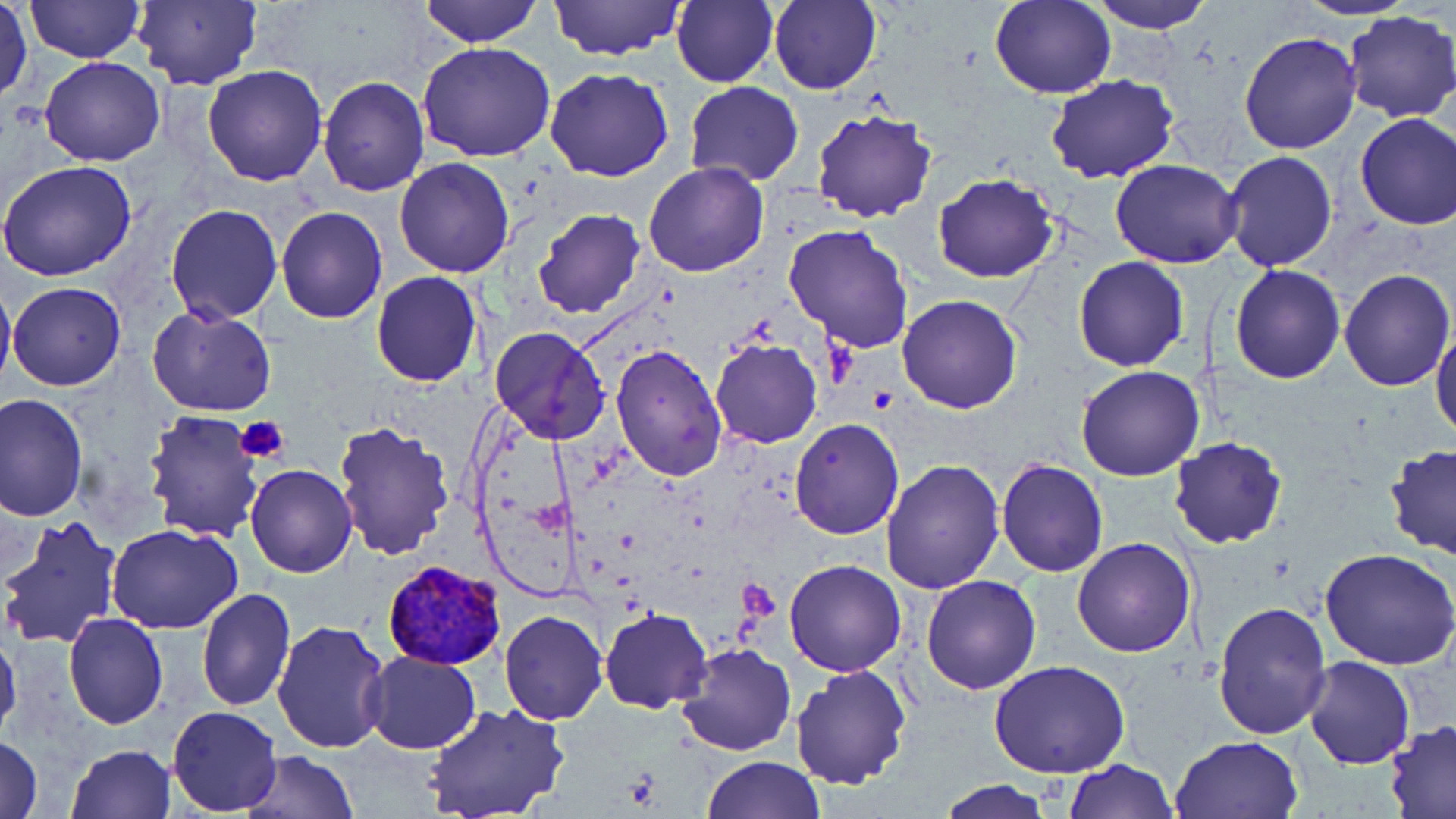
Summary:
  - Coordinate format: approximate bounding boxes as named x1/y1/x2/y2 corners in pixels
  - Plasmodium vivax-infected red blood cell locations: (x1=382, y1=561, x2=506, y2=671)
  - Platelet locations: (x1=235, y1=414, x2=290, y2=466), (x1=737, y1=576, x2=781, y2=620)
  - Uninfected red blood cell locations: (x1=23, y1=0, x2=145, y2=65), (x1=419, y1=0, x2=542, y2=47), (x1=548, y1=0, x2=685, y2=61), (x1=671, y1=0, x2=778, y2=88), (x1=989, y1=0, x2=1116, y2=99), (x1=1090, y1=0, x2=1217, y2=33), (x1=1295, y1=0, x2=1414, y2=22), (x1=131, y1=1, x2=263, y2=89), (x1=769, y1=1, x2=880, y2=94), (x1=1, y1=5, x2=33, y2=104), (x1=1343, y1=10, x2=1456, y2=124), (x1=1237, y1=32, x2=1363, y2=156), (x1=417, y1=42, x2=557, y2=162), (x1=38, y1=57, x2=166, y2=167), (x1=202, y1=64, x2=328, y2=186), (x1=544, y1=68, x2=674, y2=182), (x1=1046, y1=74, x2=1178, y2=184), (x1=317, y1=76, x2=429, y2=196), (x1=684, y1=81, x2=804, y2=187), (x1=810, y1=108, x2=939, y2=223), (x1=1354, y1=112, x2=1456, y2=232), (x1=1222, y1=151, x2=1337, y2=272), (x1=394, y1=157, x2=516, y2=277), (x1=1111, y1=159, x2=1242, y2=269), (x1=644, y1=161, x2=768, y2=277), (x1=0, y1=162, x2=137, y2=282), (x1=931, y1=174, x2=1059, y2=285), (x1=166, y1=203, x2=282, y2=323), (x1=276, y1=207, x2=387, y2=324), (x1=532, y1=208, x2=646, y2=320), (x1=783, y1=223, x2=915, y2=354), (x1=1073, y1=257, x2=1190, y2=372), (x1=1229, y1=265, x2=1345, y2=383), (x1=1337, y1=268, x2=1455, y2=392), (x1=370, y1=271, x2=482, y2=388), (x1=0, y1=272, x2=15, y2=398), (x1=8, y1=281, x2=125, y2=392), (x1=897, y1=294, x2=1022, y2=414), (x1=147, y1=305, x2=277, y2=418), (x1=491, y1=326, x2=610, y2=444), (x1=1431, y1=327, x2=1456, y2=444), (x1=710, y1=338, x2=822, y2=448), (x1=610, y1=345, x2=727, y2=483), (x1=1076, y1=365, x2=1204, y2=482), (x1=1, y1=394, x2=88, y2=520), (x1=143, y1=408, x2=267, y2=544), (x1=789, y1=417, x2=905, y2=539), (x1=333, y1=420, x2=455, y2=561), (x1=1169, y1=436, x2=1288, y2=550), (x1=1383, y1=445, x2=1456, y2=561), (x1=879, y1=458, x2=1005, y2=594), (x1=995, y1=459, x2=1108, y2=578), (x1=245, y1=464, x2=357, y2=579), (x1=0, y1=513, x2=123, y2=648), (x1=107, y1=524, x2=244, y2=635), (x1=1071, y1=536, x2=1197, y2=657), (x1=1322, y1=548, x2=1456, y2=669), (x1=784, y1=559, x2=907, y2=677), (x1=920, y1=574, x2=1041, y2=694), (x1=197, y1=590, x2=295, y2=713), (x1=1211, y1=600, x2=1331, y2=741), (x1=599, y1=608, x2=712, y2=713), (x1=500, y1=611, x2=608, y2=725), (x1=64, y1=613, x2=168, y2=728), (x1=272, y1=618, x2=393, y2=756), (x1=460, y1=621, x2=587, y2=771), (x1=0, y1=625, x2=22, y2=741), (x1=676, y1=643, x2=797, y2=755), (x1=362, y1=650, x2=480, y2=753), (x1=1303, y1=654, x2=1416, y2=770), (x1=989, y1=659, x2=1129, y2=778), (x1=790, y1=663, x2=910, y2=790), (x1=422, y1=705, x2=569, y2=819), (x1=167, y1=706, x2=281, y2=814), (x1=1382, y1=719, x2=1456, y2=815), (x1=1171, y1=735, x2=1303, y2=819), (x1=0, y1=737, x2=45, y2=818), (x1=68, y1=743, x2=175, y2=818), (x1=240, y1=749, x2=358, y2=818), (x1=701, y1=756, x2=824, y2=819), (x1=1064, y1=758, x2=1178, y2=818), (x1=936, y1=778, x2=1060, y2=818)
  - Slide-level diagnosis: Plasmodium vivax
  - Image size: 1456×819 pixels
  - Magnification: 1000x
  - Stain: May-Grünwald-Giemsa
  - Field of view: one of a larger specimen
  - Preparation: thin blood film
  - Modality: light microscopy